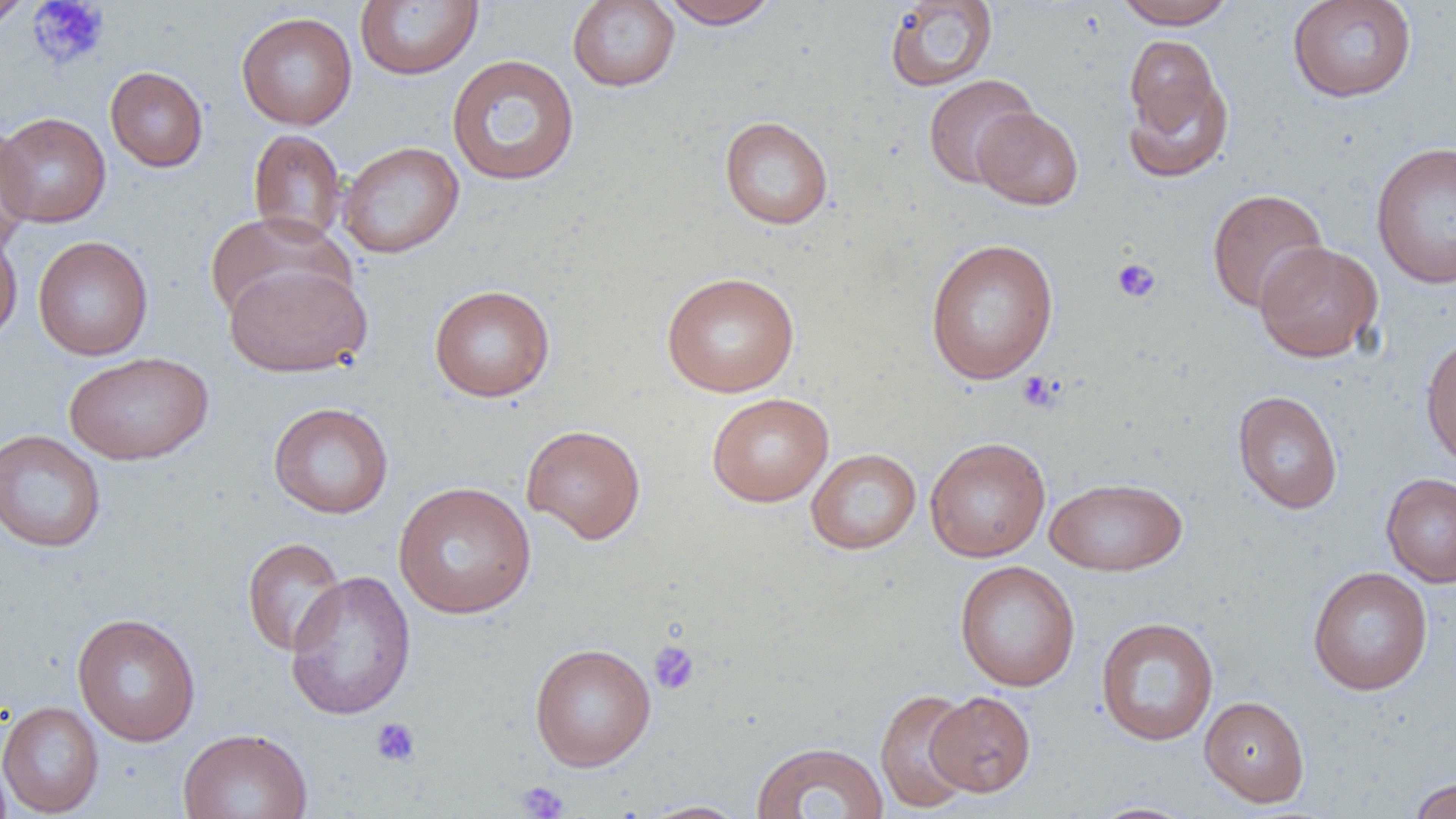
Approximate bounding boxes as named x1/y1/x2/y2 corners in pixels. Platelet locations: (x1=27, y1=0, x2=110, y2=71), (x1=1112, y1=258, x2=1162, y2=304), (x1=1016, y1=371, x2=1063, y2=412), (x1=648, y1=640, x2=700, y2=696), (x1=370, y1=717, x2=421, y2=767), (x1=515, y1=780, x2=569, y2=819). Uninfected red blood cell locations: (x1=0, y1=0, x2=35, y2=31), (x1=567, y1=0, x2=680, y2=91), (x1=659, y1=0, x2=780, y2=29), (x1=1113, y1=0, x2=1238, y2=29), (x1=1286, y1=0, x2=1418, y2=103), (x1=355, y1=1, x2=483, y2=80), (x1=883, y1=1, x2=999, y2=92), (x1=235, y1=12, x2=358, y2=130), (x1=1124, y1=35, x2=1223, y2=136), (x1=446, y1=54, x2=580, y2=186), (x1=105, y1=66, x2=209, y2=172), (x1=1123, y1=72, x2=1234, y2=184), (x1=922, y1=74, x2=1039, y2=188), (x1=972, y1=107, x2=1084, y2=209), (x1=0, y1=112, x2=111, y2=227), (x1=719, y1=116, x2=833, y2=229), (x1=0, y1=121, x2=36, y2=250), (x1=248, y1=128, x2=348, y2=245), (x1=338, y1=141, x2=465, y2=259), (x1=1370, y1=141, x2=1456, y2=289), (x1=1206, y1=188, x2=1328, y2=314), (x1=204, y1=211, x2=352, y2=325), (x1=0, y1=226, x2=23, y2=347), (x1=33, y1=235, x2=153, y2=361), (x1=924, y1=237, x2=1059, y2=385), (x1=1254, y1=240, x2=1383, y2=362), (x1=224, y1=261, x2=373, y2=378), (x1=661, y1=271, x2=800, y2=398), (x1=429, y1=284, x2=555, y2=402), (x1=1420, y1=333, x2=1456, y2=470), (x1=64, y1=352, x2=214, y2=465), (x1=1231, y1=390, x2=1343, y2=514), (x1=706, y1=393, x2=834, y2=507), (x1=268, y1=401, x2=394, y2=519), (x1=521, y1=424, x2=646, y2=544), (x1=0, y1=429, x2=106, y2=553), (x1=924, y1=437, x2=1051, y2=562), (x1=806, y1=448, x2=921, y2=554), (x1=1381, y1=472, x2=1456, y2=588), (x1=1045, y1=476, x2=1187, y2=576), (x1=393, y1=481, x2=537, y2=619), (x1=241, y1=537, x2=347, y2=657), (x1=955, y1=560, x2=1081, y2=692), (x1=1307, y1=566, x2=1433, y2=695), (x1=284, y1=570, x2=417, y2=720), (x1=72, y1=612, x2=201, y2=746), (x1=1095, y1=616, x2=1219, y2=746), (x1=529, y1=642, x2=657, y2=771), (x1=874, y1=688, x2=978, y2=813), (x1=926, y1=691, x2=1036, y2=797), (x1=1199, y1=695, x2=1310, y2=807), (x1=0, y1=700, x2=104, y2=817), (x1=178, y1=728, x2=313, y2=819), (x1=749, y1=741, x2=890, y2=819), (x1=0, y1=751, x2=14, y2=819), (x1=1407, y1=777, x2=1456, y2=819), (x1=635, y1=800, x2=751, y2=818), (x1=1085, y1=801, x2=1200, y2=819). Slide-level diagnosis: negative for blood parasites. Single field of view. Image is 1456×819 pixels. Light microscopy. Thin blood film. Captured at 1000x magnification.